Give the extent of all Plasmodium vivax-infected red blood cells.
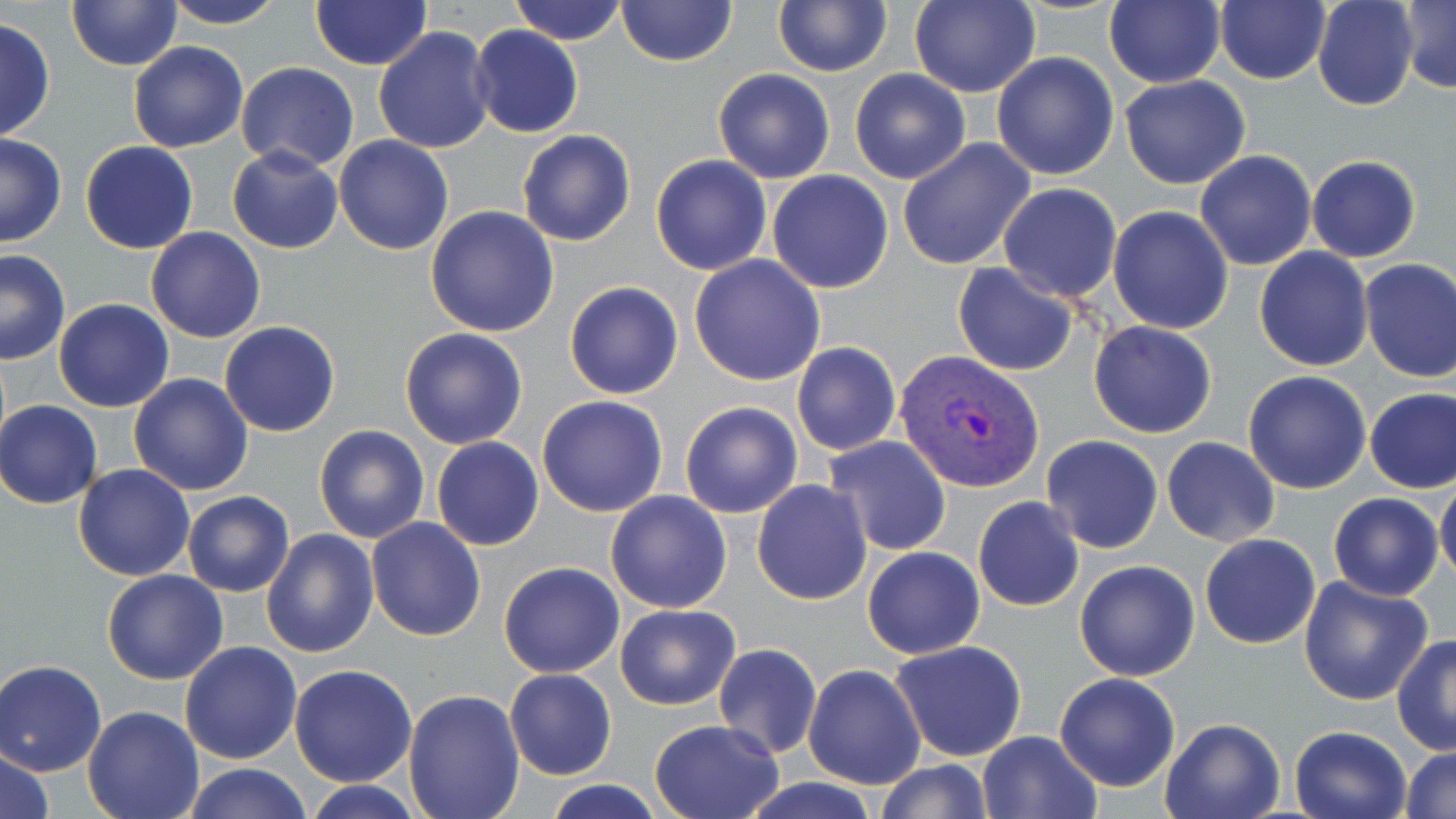

Approximate bounding boxes as named x1/y1/x2/y2 corners in pixels.
Plasmodium vivax-infected red blood cells: (x1=896, y1=349, x2=1045, y2=494).

{
  "slide_level_diagnosis": "Plasmodium vivax",
  "stain": "May-Grünwald-Giemsa",
  "magnification": "1000x",
  "image_size": "1456×819 pixels",
  "preparation": "thin blood film",
  "uninfected_red_blood_cell_locations": "approximate bounding boxes as named x1/y1/x2/y2 corners in pixels: (x1=160, y1=0, x2=288, y2=29), (x1=310, y1=0, x2=431, y2=72), (x1=507, y1=0, x2=628, y2=45), (x1=908, y1=0, x2=1040, y2=99), (x1=1105, y1=0, x2=1226, y2=90), (x1=1213, y1=0, x2=1329, y2=86), (x1=1312, y1=0, x2=1418, y2=111), (x1=1400, y1=0, x2=1456, y2=93), (x1=67, y1=1, x2=183, y2=71), (x1=616, y1=1, x2=737, y2=67), (x1=772, y1=1, x2=892, y2=76), (x1=0, y1=16, x2=55, y2=141), (x1=468, y1=25, x2=583, y2=138), (x1=372, y1=26, x2=493, y2=155), (x1=128, y1=41, x2=249, y2=152), (x1=992, y1=52, x2=1119, y2=179), (x1=237, y1=62, x2=361, y2=172), (x1=712, y1=67, x2=835, y2=183), (x1=849, y1=68, x2=972, y2=184), (x1=1119, y1=75, x2=1251, y2=190), (x1=517, y1=129, x2=635, y2=246), (x1=0, y1=131, x2=67, y2=247), (x1=334, y1=135, x2=454, y2=256), (x1=897, y1=138, x2=1036, y2=271), (x1=80, y1=140, x2=199, y2=254), (x1=227, y1=145, x2=343, y2=254), (x1=1195, y1=149, x2=1317, y2=272), (x1=651, y1=154, x2=773, y2=276), (x1=1306, y1=154, x2=1422, y2=263), (x1=767, y1=171, x2=894, y2=293), (x1=997, y1=183, x2=1123, y2=302), (x1=426, y1=205, x2=559, y2=337), (x1=1108, y1=206, x2=1235, y2=335), (x1=146, y1=227, x2=266, y2=344), (x1=1255, y1=248, x2=1374, y2=371), (x1=0, y1=250, x2=71, y2=364), (x1=688, y1=255, x2=826, y2=388), (x1=1358, y1=258, x2=1456, y2=383), (x1=952, y1=263, x2=1079, y2=378), (x1=564, y1=281, x2=684, y2=399), (x1=54, y1=298, x2=174, y2=412), (x1=1088, y1=320, x2=1218, y2=438), (x1=220, y1=321, x2=340, y2=437), (x1=400, y1=327, x2=528, y2=448), (x1=792, y1=342, x2=901, y2=457), (x1=1243, y1=370, x2=1373, y2=494), (x1=128, y1=374, x2=254, y2=496), (x1=1365, y1=387, x2=1456, y2=494), (x1=538, y1=395, x2=669, y2=517), (x1=0, y1=400, x2=103, y2=508), (x1=678, y1=400, x2=802, y2=519), (x1=314, y1=424, x2=430, y2=544), (x1=824, y1=435, x2=952, y2=557), (x1=1041, y1=435, x2=1162, y2=555), (x1=431, y1=437, x2=544, y2=550), (x1=1161, y1=438, x2=1279, y2=546), (x1=74, y1=464, x2=195, y2=583), (x1=751, y1=479, x2=872, y2=605), (x1=1435, y1=481, x2=1456, y2=585), (x1=604, y1=489, x2=732, y2=613), (x1=183, y1=491, x2=295, y2=597), (x1=1328, y1=493, x2=1444, y2=601), (x1=972, y1=496, x2=1084, y2=612), (x1=366, y1=517, x2=486, y2=641), (x1=260, y1=528, x2=379, y2=660), (x1=1199, y1=533, x2=1321, y2=649), (x1=861, y1=545, x2=984, y2=659), (x1=1074, y1=560, x2=1200, y2=681), (x1=498, y1=562, x2=624, y2=679), (x1=101, y1=569, x2=229, y2=685), (x1=1299, y1=574, x2=1434, y2=705), (x1=614, y1=604, x2=740, y2=710), (x1=1391, y1=635, x2=1456, y2=755), (x1=889, y1=640, x2=1027, y2=761), (x1=179, y1=641, x2=302, y2=764), (x1=711, y1=642, x2=823, y2=760), (x1=0, y1=658, x2=107, y2=776), (x1=803, y1=663, x2=927, y2=790), (x1=289, y1=664, x2=418, y2=786), (x1=504, y1=668, x2=616, y2=780), (x1=1054, y1=672, x2=1181, y2=793), (x1=403, y1=687, x2=526, y2=818), (x1=82, y1=706, x2=203, y2=819), (x1=1160, y1=717, x2=1284, y2=819), (x1=648, y1=718, x2=784, y2=818), (x1=1289, y1=725, x2=1414, y2=819), (x1=977, y1=730, x2=1101, y2=818), (x1=1, y1=745, x2=55, y2=819), (x1=1402, y1=746, x2=1456, y2=818), (x1=873, y1=759, x2=996, y2=818), (x1=181, y1=763, x2=315, y2=819), (x1=541, y1=778, x2=667, y2=818), (x1=300, y1=779, x2=429, y2=818), (x1=743, y1=779, x2=881, y2=817)",
  "modality": "optical microscopy",
  "field_of_view": "single"
}